Identify the parasite.
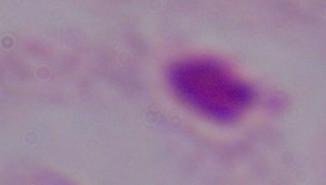
A trichomonad.

modality = photomicrograph
magnification = 1000x